Assess this cell for malaria.
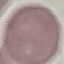
It is uninfected.

preparation = thin smear
image type = cell patch, automatically extracted from a larger field of view and resized to 64 × 64 pixels
capture = smartphone through the microscope eyepiece
stain = Giemsa